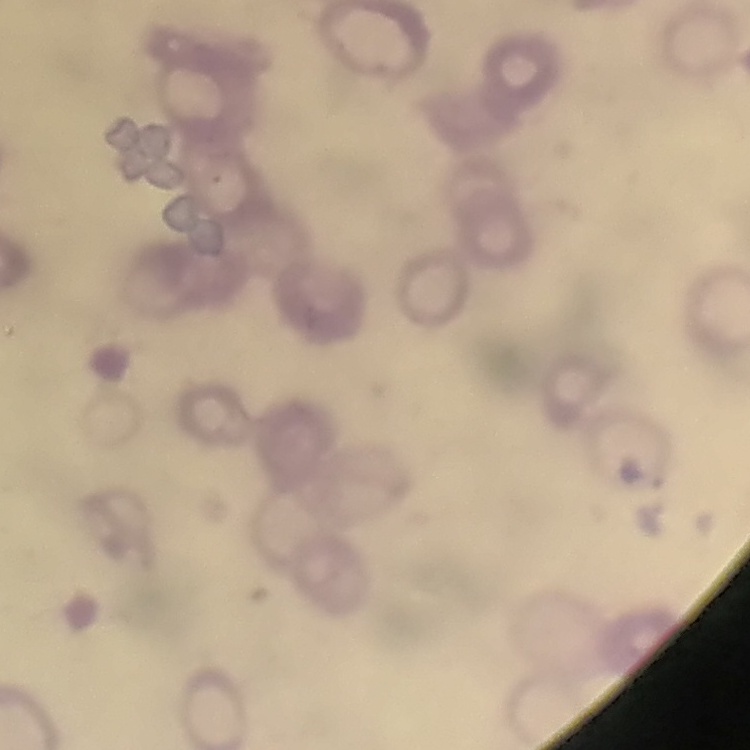

red blood cell morphology = rouleaux formation
image type = square crop of a larger photomicrograph
preparation = thin blood smear
stain = Field's or Giemsa